State which parasite is depicted.
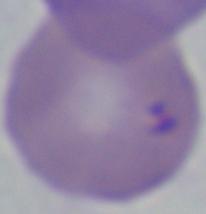

Babesia.

Captured at 1000x magnification. Micrograph.